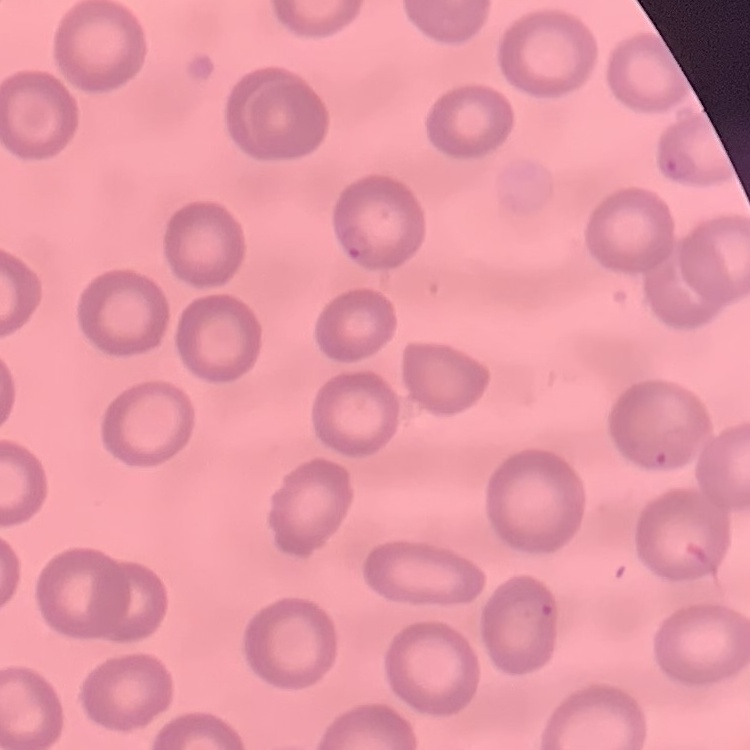

red blood cell morphology = no rouleaux formation
preparation = thin blood smear
image type = one tile cut from a larger photomicrograph
stain = Field's or Giemsa